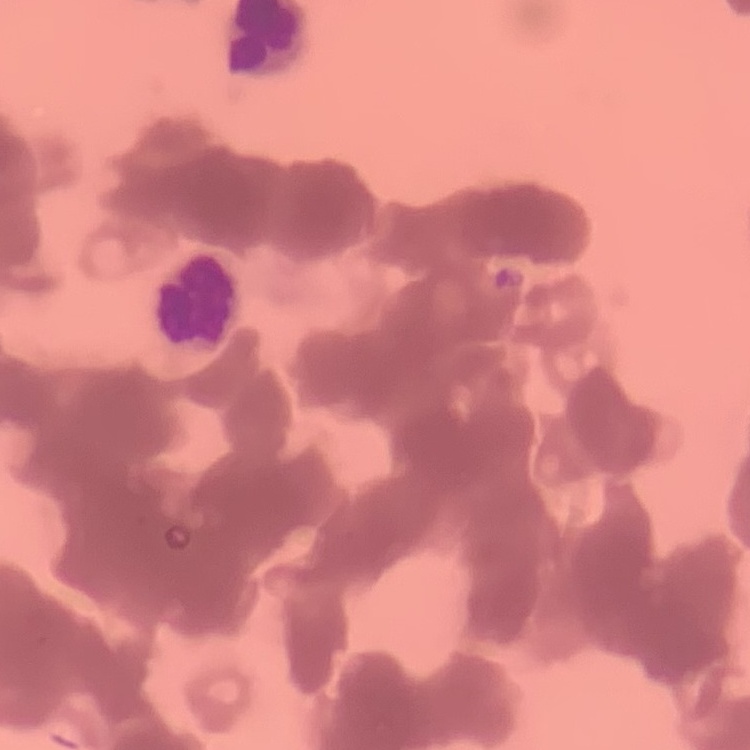
The erythrocytes show rouleaux formation. Thin blood smear. Stained with either Field's or Giemsa. One tile cut from a larger photomicrograph.